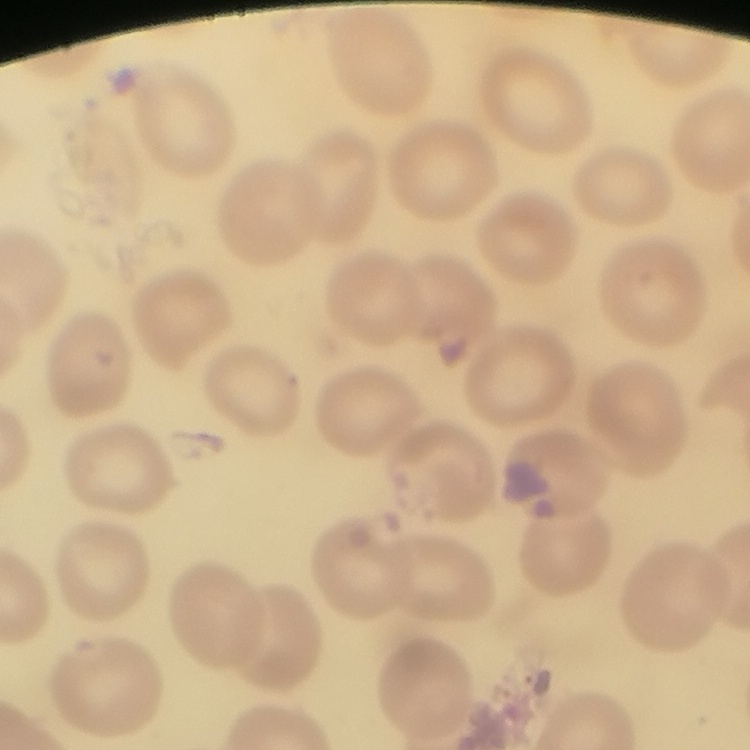
Summary:
  - Erythrocyte morphology: no rouleaux formation
  - Preparation: thin peripheral smear
  - Stain: Field's or Giemsa
  - Image type: square crop of a larger photomicrograph